Locate the P. falciparum-infected red blood cells and any of indeterminate infection status.
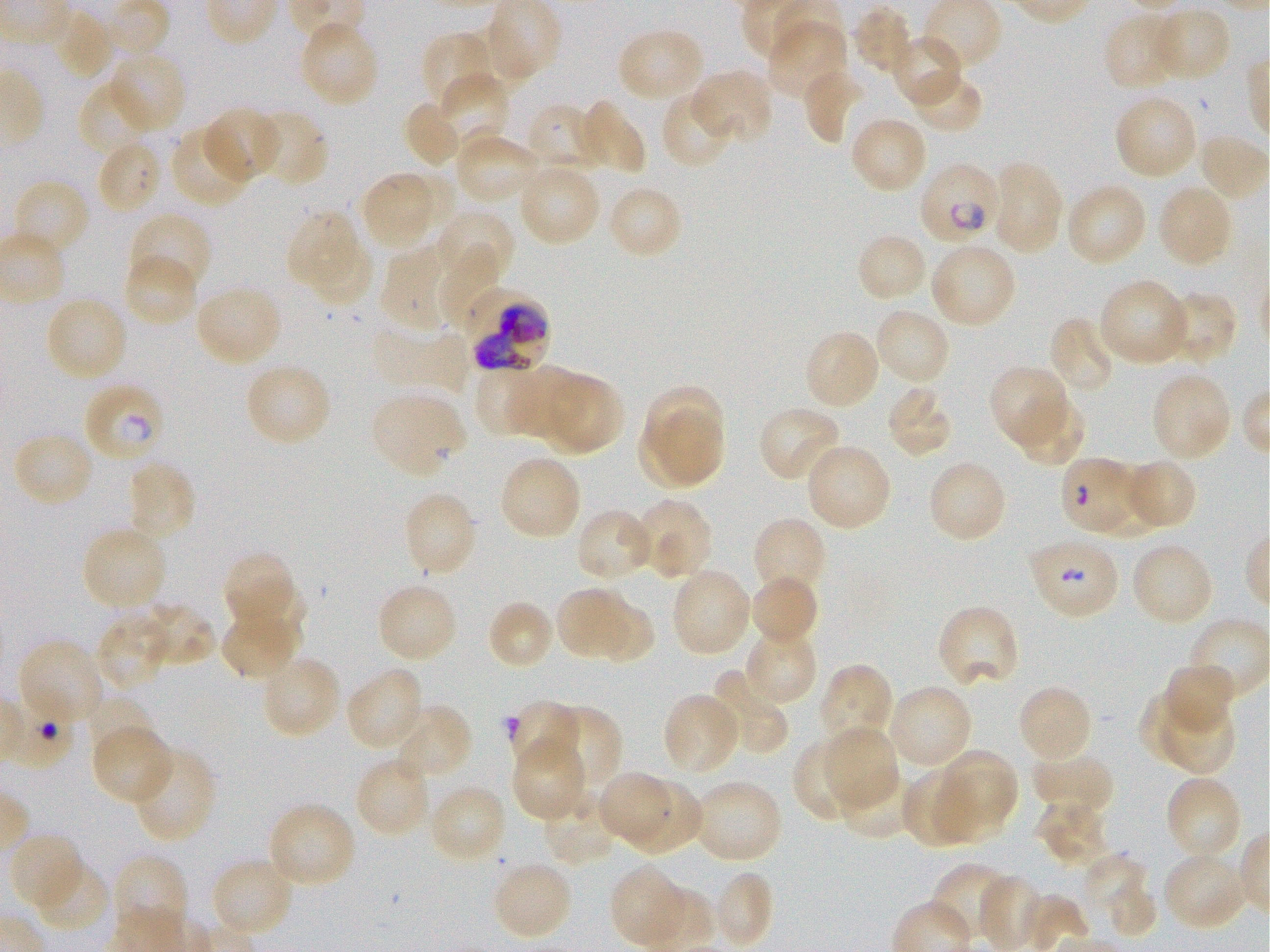
Approximate bounding boxes as [x1, y1, x2, y2] in pixels. Not every red blood cell is marked. A life-cycle stage — or a range of stages, where the recorded stages span more than one — follows each staged infected red blood cell.
Infected red blood cells: [96, 139, 162, 214] early ring; [917, 162, 1002, 245] early ring to early trophozoite; [464, 290, 551, 375]; [87, 386, 161, 460] early ring to late trophozoite; [1059, 456, 1135, 532] early ring.
Red blood cells of indeterminate infection status: [1029, 543, 1115, 617].

Summary:
  - Locations of uninfected red blood cells: [492, 0, 560, 73], [852, 5, 916, 77], [1150, 6, 1233, 83], [52, 11, 115, 81], [1102, 13, 1180, 91], [298, 20, 380, 108], [765, 21, 848, 102], [456, 22, 526, 90], [617, 27, 705, 103], [420, 30, 497, 111], [891, 35, 963, 109], [110, 52, 186, 134], [802, 68, 866, 146], [909, 69, 984, 134], [690, 70, 773, 146], [438, 73, 510, 153], [78, 80, 155, 156], [660, 90, 735, 170], [1114, 94, 1198, 180], [402, 98, 462, 168], [576, 99, 647, 176], [524, 103, 601, 173], [203, 107, 282, 183], [255, 108, 330, 189], [849, 116, 928, 195], [170, 125, 252, 209], [454, 132, 541, 205], [1197, 133, 1270, 200], [517, 162, 601, 246], [989, 162, 1064, 255], [367, 172, 434, 244], [12, 179, 91, 260], [1064, 181, 1148, 267], [1157, 183, 1234, 268], [607, 184, 684, 261], [435, 208, 516, 285], [287, 211, 355, 285], [128, 212, 213, 294], [855, 232, 929, 305], [308, 233, 372, 306], [436, 242, 502, 331], [929, 243, 1017, 329], [380, 247, 444, 333], [122, 254, 198, 328], [1098, 278, 1191, 367], [195, 286, 283, 367], [1160, 290, 1238, 367], [44, 294, 129, 381], [873, 308, 952, 387], [1049, 315, 1117, 396], [373, 328, 470, 392], [803, 329, 881, 411], [244, 361, 331, 448], [989, 364, 1069, 447], [505, 365, 586, 440], [472, 368, 538, 439], [1150, 371, 1232, 461], [539, 372, 624, 455], [645, 387, 723, 458], [884, 387, 955, 460], [370, 392, 465, 476], [1012, 395, 1086, 467], [757, 405, 843, 483], [657, 408, 722, 484], [637, 417, 706, 489], [12, 431, 95, 508], [804, 443, 893, 532], [499, 455, 583, 541], [1127, 458, 1197, 527], [927, 459, 1007, 544], [126, 461, 198, 542], [1089, 462, 1165, 536], [401, 490, 478, 577], [634, 498, 713, 579], [574, 507, 654, 583], [751, 516, 827, 600], [80, 526, 168, 611], [1130, 542, 1215, 626], [222, 552, 296, 635], [670, 567, 753, 657], [747, 573, 819, 649], [227, 578, 305, 658], [375, 582, 460, 663], [555, 587, 632, 661], [586, 596, 654, 664], [485, 599, 556, 671], [138, 600, 217, 669], [935, 604, 1020, 690], [219, 609, 299, 680], [95, 613, 170, 691], [743, 628, 818, 706], [18, 638, 105, 724], [261, 656, 342, 739], [1163, 661, 1233, 736], [818, 663, 895, 749], [345, 665, 424, 752], [709, 667, 789, 755], [1016, 683, 1094, 763], [887, 684, 974, 770], [1140, 692, 1208, 763], [661, 693, 740, 774], [1162, 694, 1237, 774], [86, 696, 154, 761], [507, 700, 579, 773], [391, 703, 473, 781], [542, 704, 621, 790], [823, 725, 899, 811], [93, 729, 175, 806], [513, 739, 588, 822], [791, 740, 865, 826], [132, 747, 217, 844], [944, 748, 1019, 819], [1031, 752, 1115, 816], [354, 756, 432, 838], [837, 766, 914, 839], [902, 769, 982, 849], [935, 769, 1012, 843], [598, 772, 671, 847], [1164, 775, 1243, 861], [627, 779, 704, 855], [692, 779, 782, 864], [429, 784, 507, 864], [542, 793, 619, 866], [1035, 800, 1111, 868], [267, 801, 356, 889], [9, 833, 85, 911], [1085, 851, 1145, 907], [1162, 851, 1247, 931], [113, 855, 190, 936], [211, 857, 295, 939], [34, 858, 110, 934], [491, 859, 574, 941], [608, 864, 688, 948], [930, 864, 1015, 944], [710, 870, 775, 949], [979, 875, 1046, 952], [1106, 878, 1158, 939]
  - Preparation: thin blood smear
  - Field of view: one from this slide
  - Culture: P. falciparum strain 3D7, static, in vitro
  - Donor blood group: O+
  - Stain: Giemsa
  - Objective: 100x, oil immersion, numerical aperture 1.25
  - Image size: 1270×952 pixels